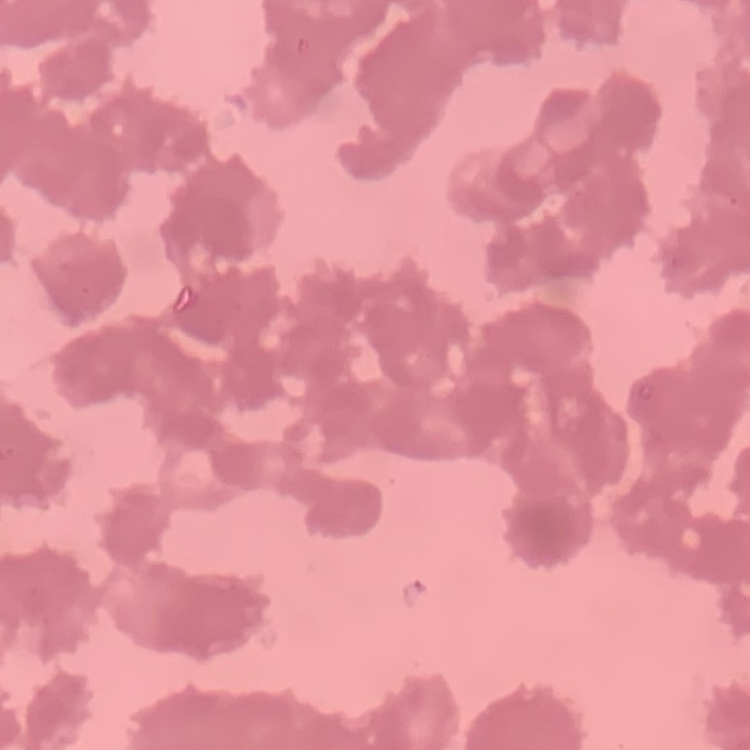
Summary:
  - Red blood cell morphology: rouleaux formation
  - Preparation: thin blood smear
  - Image type: square crop of a larger photomicrograph
  - Stain: Field's or Giemsa